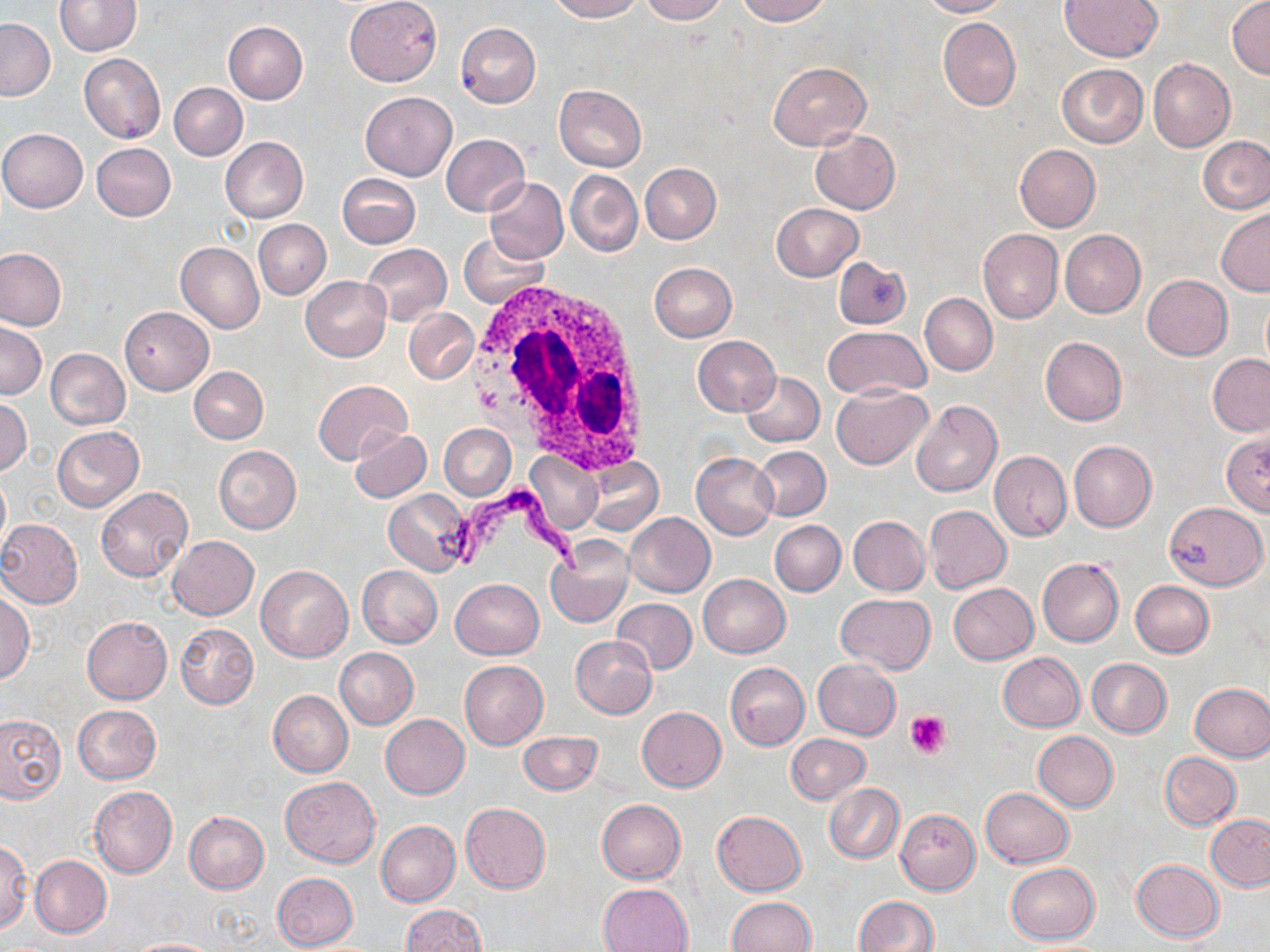
Summary:
  - Coordinate format: approximate bounding boxes as named x1/y1/x2/y2 corners in pixels
  - Platelet locations: (x1=905, y1=711, x2=950, y2=758)
  - Uninfected red blood cell locations: (x1=547, y1=0, x2=645, y2=21), (x1=641, y1=0, x2=727, y2=23), (x1=735, y1=0, x2=832, y2=25), (x1=917, y1=0, x2=1008, y2=17), (x1=1060, y1=0, x2=1163, y2=61), (x1=1227, y1=0, x2=1269, y2=78), (x1=54, y1=1, x2=141, y2=56), (x1=345, y1=1, x2=442, y2=86), (x1=939, y1=18, x2=1020, y2=110), (x1=0, y1=19, x2=55, y2=100), (x1=223, y1=22, x2=307, y2=104), (x1=455, y1=22, x2=540, y2=108), (x1=79, y1=53, x2=166, y2=144), (x1=1147, y1=58, x2=1236, y2=152), (x1=769, y1=62, x2=870, y2=150), (x1=1057, y1=64, x2=1148, y2=147), (x1=169, y1=83, x2=247, y2=160), (x1=554, y1=84, x2=647, y2=171), (x1=360, y1=91, x2=456, y2=182), (x1=810, y1=128, x2=900, y2=214), (x1=0, y1=129, x2=88, y2=213), (x1=440, y1=134, x2=530, y2=216), (x1=220, y1=137, x2=308, y2=223), (x1=1199, y1=137, x2=1270, y2=214), (x1=91, y1=143, x2=176, y2=221), (x1=1014, y1=144, x2=1100, y2=232), (x1=640, y1=163, x2=721, y2=244), (x1=565, y1=169, x2=642, y2=257), (x1=336, y1=174, x2=420, y2=248), (x1=485, y1=176, x2=569, y2=263), (x1=772, y1=203, x2=863, y2=281), (x1=1216, y1=209, x2=1270, y2=295), (x1=253, y1=219, x2=330, y2=299), (x1=978, y1=229, x2=1062, y2=323), (x1=1059, y1=230, x2=1145, y2=318), (x1=459, y1=232, x2=548, y2=308), (x1=176, y1=242, x2=264, y2=334), (x1=360, y1=244, x2=453, y2=326), (x1=0, y1=248, x2=65, y2=330), (x1=833, y1=255, x2=911, y2=329), (x1=649, y1=262, x2=737, y2=341), (x1=1141, y1=275, x2=1232, y2=360), (x1=300, y1=276, x2=391, y2=361), (x1=920, y1=293, x2=998, y2=376), (x1=119, y1=307, x2=213, y2=394), (x1=404, y1=309, x2=478, y2=384), (x1=0, y1=321, x2=47, y2=398), (x1=822, y1=327, x2=930, y2=400), (x1=692, y1=335, x2=780, y2=416), (x1=1040, y1=337, x2=1127, y2=425), (x1=45, y1=349, x2=130, y2=430), (x1=1207, y1=354, x2=1270, y2=436), (x1=188, y1=366, x2=268, y2=444), (x1=739, y1=371, x2=824, y2=447), (x1=312, y1=379, x2=411, y2=465), (x1=831, y1=383, x2=932, y2=468), (x1=0, y1=397, x2=31, y2=475), (x1=910, y1=399, x2=1002, y2=497), (x1=440, y1=423, x2=515, y2=500), (x1=53, y1=426, x2=144, y2=513), (x1=348, y1=428, x2=431, y2=503), (x1=1220, y1=431, x2=1270, y2=517), (x1=1069, y1=440, x2=1156, y2=532), (x1=214, y1=445, x2=301, y2=533), (x1=753, y1=445, x2=831, y2=521), (x1=526, y1=451, x2=602, y2=535), (x1=989, y1=451, x2=1071, y2=540), (x1=691, y1=452, x2=778, y2=539), (x1=584, y1=457, x2=662, y2=535), (x1=0, y1=472, x2=10, y2=553), (x1=96, y1=487, x2=193, y2=582), (x1=384, y1=489, x2=473, y2=575), (x1=1164, y1=502, x2=1267, y2=590), (x1=924, y1=505, x2=1011, y2=593), (x1=625, y1=513, x2=715, y2=597), (x1=849, y1=516, x2=929, y2=596), (x1=0, y1=519, x2=84, y2=608), (x1=770, y1=521, x2=845, y2=596), (x1=168, y1=535, x2=258, y2=619), (x1=546, y1=537, x2=634, y2=629), (x1=1037, y1=558, x2=1124, y2=646), (x1=256, y1=565, x2=353, y2=662), (x1=357, y1=566, x2=442, y2=647), (x1=698, y1=573, x2=789, y2=658), (x1=450, y1=578, x2=542, y2=659), (x1=1130, y1=580, x2=1213, y2=657), (x1=949, y1=583, x2=1038, y2=663), (x1=0, y1=593, x2=34, y2=682), (x1=835, y1=594, x2=934, y2=674), (x1=612, y1=599, x2=698, y2=674), (x1=82, y1=617, x2=172, y2=704), (x1=177, y1=623, x2=258, y2=708), (x1=572, y1=635, x2=656, y2=718), (x1=334, y1=648, x2=419, y2=729), (x1=997, y1=653, x2=1085, y2=732), (x1=1087, y1=658, x2=1171, y2=737), (x1=460, y1=660, x2=548, y2=749), (x1=813, y1=660, x2=901, y2=739), (x1=724, y1=662, x2=809, y2=749), (x1=1190, y1=682, x2=1270, y2=762), (x1=268, y1=690, x2=354, y2=778), (x1=73, y1=704, x2=161, y2=785), (x1=638, y1=706, x2=726, y2=792), (x1=0, y1=714, x2=65, y2=801), (x1=380, y1=714, x2=469, y2=799), (x1=517, y1=731, x2=603, y2=795), (x1=1033, y1=731, x2=1118, y2=811), (x1=786, y1=733, x2=871, y2=804), (x1=1160, y1=752, x2=1241, y2=829), (x1=280, y1=776, x2=380, y2=867), (x1=824, y1=784, x2=903, y2=863), (x1=89, y1=786, x2=176, y2=877), (x1=980, y1=788, x2=1074, y2=868), (x1=597, y1=799, x2=685, y2=883), (x1=460, y1=803, x2=550, y2=893), (x1=896, y1=809, x2=982, y2=895), (x1=184, y1=811, x2=269, y2=893), (x1=711, y1=811, x2=806, y2=896), (x1=1205, y1=815, x2=1270, y2=890), (x1=375, y1=819, x2=460, y2=907), (x1=0, y1=839, x2=31, y2=932), (x1=29, y1=854, x2=111, y2=938), (x1=1131, y1=859, x2=1223, y2=942), (x1=1004, y1=863, x2=1099, y2=944), (x1=271, y1=872, x2=359, y2=950), (x1=598, y1=882, x2=693, y2=952), (x1=854, y1=896, x2=938, y2=951), (x1=727, y1=897, x2=815, y2=951), (x1=399, y1=904, x2=486, y2=952), (x1=124, y1=938, x2=221, y2=951)
  - Trypanosoma brucei locations: (x1=436, y1=480, x2=590, y2=572)
  - White blood cell locations: (x1=466, y1=275, x2=651, y2=475)
  - Slide-level diagnosis: Trypanosoma brucei
  - Modality: light microscopy
  - Magnification: 1000x
  - Preparation: thin blood smear
  - Image size: 1270×952 pixels
  - Field of view: single
  - Stain: May-Grünwald-Giemsa